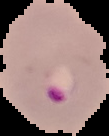
Summary:
  - Image type: segmented cell region with the area outside set to black
  - Malaria status: parasitized
  - Preparation: thin blood film
  - Image size: 109×136 pixels